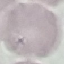
malaria_status: uninfected
stain: Giemsa
capture: smartphone camera at the microscope eyepiece
preparation: thin blood smear
image_type: cell patch, automatically extracted from a larger field of view and resized to 64 × 64 pixels